Name the blood parasite species.
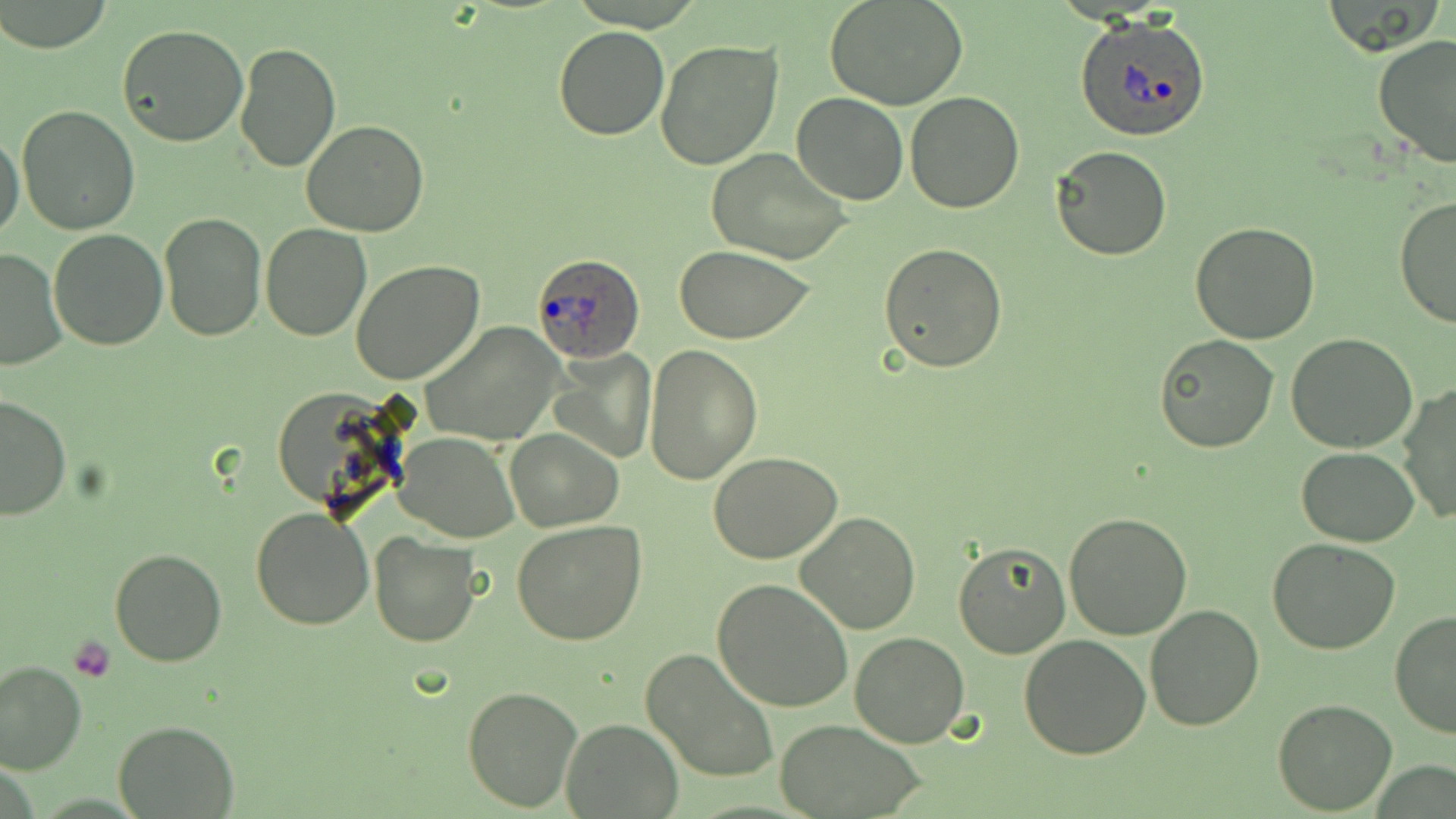
Plasmodium ovale.

Approximate bounding boxes as (x1, y1, x2, y2) in pixels. Platelet locations: (71, 635, 116, 683). Uninfected red blood cell locations: (825, 1, 969, 110), (116, 23, 250, 149), (553, 26, 671, 142), (1372, 34, 1456, 166), (233, 40, 341, 174), (655, 40, 784, 171), (792, 92, 907, 205), (904, 92, 1024, 213), (17, 104, 140, 233), (301, 120, 430, 237), (1, 132, 25, 245), (1051, 144, 1175, 260), (707, 148, 854, 265), (1393, 195, 1456, 329), (159, 212, 266, 339), (1190, 221, 1320, 345), (259, 224, 371, 341), (47, 228, 168, 350), (877, 243, 1008, 373), (675, 246, 816, 343), (0, 247, 68, 373), (351, 260, 484, 386), (419, 323, 567, 447), (1156, 334, 1279, 453), (1285, 334, 1419, 454), (644, 345, 763, 484), (549, 348, 658, 463), (1398, 382, 1456, 526), (0, 394, 72, 522), (506, 430, 621, 531), (396, 432, 518, 542), (1297, 447, 1420, 546), (709, 452, 841, 563), (250, 507, 376, 630), (1062, 512, 1192, 640), (795, 513, 921, 634), (511, 521, 646, 646), (369, 533, 479, 648), (1267, 539, 1401, 656), (953, 540, 1070, 659), (109, 546, 227, 666), (712, 578, 854, 713), (1144, 603, 1266, 732), (1389, 610, 1456, 740), (848, 632, 970, 747), (1018, 632, 1151, 759), (641, 650, 778, 783), (0, 660, 86, 774), (461, 685, 582, 813), (1271, 699, 1397, 814), (561, 718, 683, 818), (775, 718, 928, 817), (112, 721, 239, 817). Plasmodium ovale-infected red blood cell locations: (1074, 14, 1212, 143), (530, 252, 646, 365). Optical microscopy. May-Grünwald-Giemsa-stained preparation. Captured at 1000x magnification. Image is 1456×819 pixels. One field of a larger specimen. Thin blood smear.